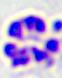

Summary:
  - Magnification: 400x
  - Modality: micrograph
  - Identification: white blood cell